Classify this cell by malaria status.
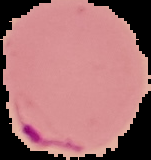
It is parasitized.

Image is 151×160 pixels. From a thin blood film. Cell region segmented out of the field of view; the surrounding area is masked to black.